Locate every blood parasite and identify its species.
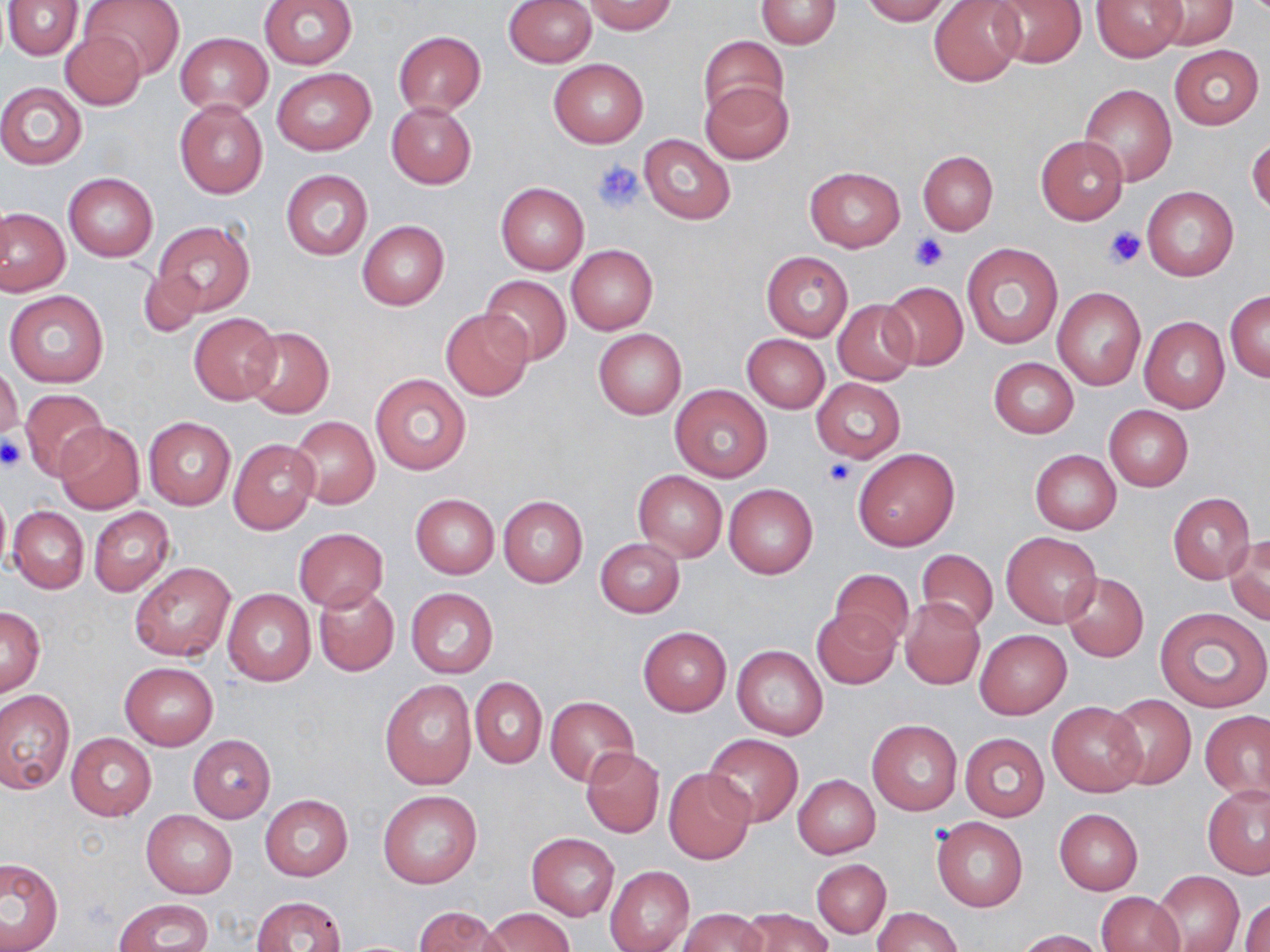

No blood parasites observed.

Approximate bounding boxes as [x1, y1, x2, y2] in pixels. Platelet locations: [592, 159, 643, 213], [1104, 226, 1145, 269], [911, 233, 946, 271], [0, 438, 25, 473], [823, 457, 858, 488]. Uninfected red blood cell locations: [3, 0, 82, 60], [80, 0, 185, 80], [258, 0, 358, 68], [755, 0, 842, 48], [861, 0, 951, 25], [928, 0, 1026, 87], [987, 0, 1086, 69], [1091, 0, 1187, 62], [1152, 0, 1237, 50], [504, 1, 597, 66], [584, 2, 678, 35], [58, 30, 146, 111], [393, 31, 486, 116], [176, 32, 272, 115], [699, 35, 788, 119], [1169, 45, 1264, 129], [548, 58, 648, 148], [271, 68, 376, 155], [701, 80, 793, 164], [0, 83, 87, 167], [1080, 84, 1177, 185], [175, 99, 268, 198], [386, 102, 476, 188], [639, 134, 736, 224], [1035, 134, 1128, 225], [1247, 137, 1270, 215], [918, 150, 998, 234], [805, 167, 904, 251], [281, 170, 372, 260], [63, 173, 158, 262], [496, 181, 589, 275], [1142, 186, 1239, 282], [1, 209, 70, 295], [154, 220, 254, 316], [357, 220, 449, 310], [961, 243, 1062, 350], [566, 245, 658, 334], [761, 250, 853, 341], [137, 268, 205, 338], [481, 275, 571, 364], [880, 281, 968, 371], [1052, 288, 1146, 390], [4, 289, 109, 388], [1226, 291, 1269, 382], [833, 300, 919, 386], [441, 308, 534, 400], [189, 312, 281, 405], [1140, 317, 1229, 413], [243, 326, 334, 417], [593, 328, 685, 419], [742, 334, 830, 412], [989, 357, 1079, 438], [0, 363, 22, 442], [369, 371, 471, 475], [812, 378, 906, 463], [671, 384, 773, 482], [21, 388, 108, 480], [1103, 404, 1193, 492], [289, 416, 379, 509], [145, 417, 235, 509], [54, 422, 145, 513], [228, 438, 318, 534], [854, 449, 959, 550], [1030, 450, 1121, 534], [632, 471, 727, 563], [724, 483, 818, 578], [0, 485, 10, 577], [1166, 492, 1255, 583], [410, 494, 498, 578], [497, 495, 587, 589], [8, 506, 90, 594], [88, 506, 174, 596], [292, 528, 388, 612], [1002, 531, 1101, 628], [1226, 533, 1269, 623], [595, 539, 685, 617], [916, 549, 998, 632], [128, 561, 237, 662], [830, 567, 914, 650], [1062, 572, 1149, 662], [314, 585, 399, 676], [223, 588, 315, 685], [406, 588, 499, 678], [899, 598, 985, 690], [0, 607, 45, 696], [813, 607, 900, 689], [1156, 607, 1270, 713], [638, 626, 731, 715], [974, 629, 1071, 719], [733, 645, 828, 740], [119, 662, 218, 749], [471, 677, 547, 768], [380, 679, 476, 789], [0, 691, 74, 795], [1106, 693, 1196, 789], [545, 696, 638, 785], [1047, 701, 1146, 796], [1201, 710, 1270, 801], [867, 718, 963, 816], [66, 732, 156, 820], [960, 733, 1049, 821], [703, 734, 803, 828], [187, 735, 276, 822], [582, 747, 664, 837], [665, 767, 755, 864], [793, 774, 880, 858], [1203, 785, 1270, 878], [378, 789, 482, 888], [260, 795, 352, 881], [1054, 808, 1143, 895], [141, 809, 237, 898], [932, 816, 1028, 912], [527, 833, 619, 920], [0, 856, 63, 952], [812, 859, 891, 938], [605, 866, 694, 952], [1152, 870, 1244, 952], [1096, 891, 1184, 952], [251, 895, 345, 952], [1242, 898, 1270, 952], [114, 899, 214, 951], [414, 906, 506, 952], [873, 906, 962, 952], [482, 907, 577, 951], [740, 907, 832, 952], [680, 908, 766, 952], [1015, 928, 1104, 951]. Slide-level diagnosis: no evidence of blood parasites. Thin blood smear. Single field of view. Image is 1270×952 pixels. May-Grünwald-Giemsa-stained preparation. Light microscopy. Captured at 1000x magnification.